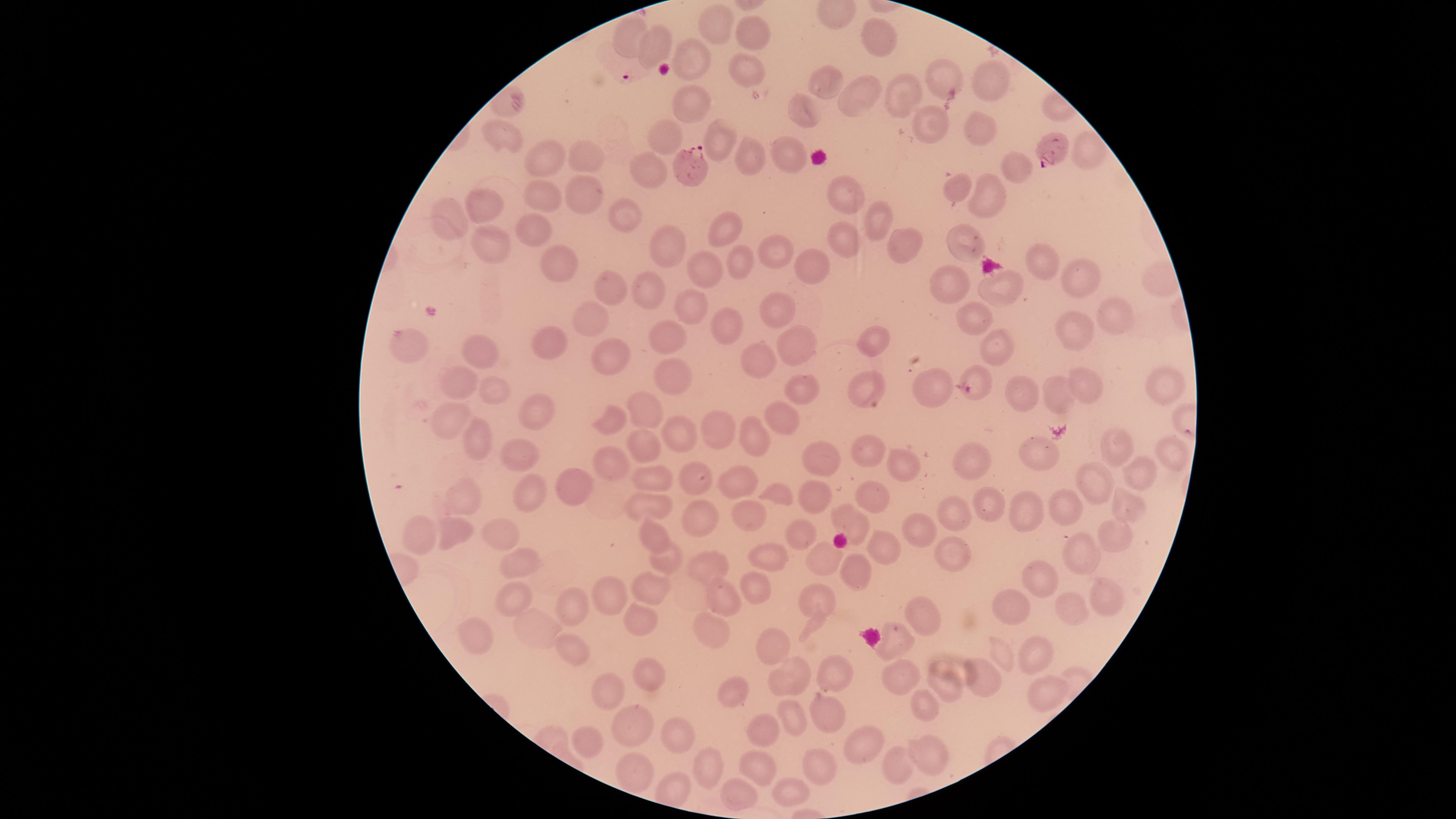
Approximate marker points as {x, y} in pixels. Uninfected RBCs: {716, 24}, {628, 34}, {751, 35}, {882, 37}, {658, 43}, {694, 59}, {746, 70}, {826, 79}, {947, 79}, {991, 81}, {865, 94}, {895, 95}, {691, 106}, {807, 112}, {936, 125}, {981, 126}, {497, 136}, {716, 136}, {662, 137}, {1090, 147}, {790, 151}, {584, 154}, {747, 157}, {546, 161}, {1010, 164}, {653, 172}, {962, 187}, {848, 192}, {580, 193}, {988, 196}, {539, 201}, {486, 205}, {621, 219}, {873, 219}, {453, 222}, {729, 231}, {531, 234}, {847, 236}, {967, 236}, {905, 241}, {494, 242}, {669, 250}, {777, 253}, {1034, 256}, {561, 263}, {738, 263}, {817, 266}, {710, 271}, {1087, 276}, {956, 282}, {1002, 282}, {614, 285}, {657, 286}, {695, 305}, {775, 313}, {975, 315}, {1110, 318}, {589, 324}, {723, 326}, {1075, 330}, {667, 337}, {873, 341}, {792, 343}, {995, 344}, {554, 345}, {410, 348}, {474, 353}, {614, 356}, {762, 359}, {675, 372}, {975, 375}, {1085, 383}, {1156, 383}, {805, 385}, {870, 385}, {461, 386}, {933, 388}, {501, 391}, {1057, 392}, {1023, 393}, {544, 404}, {783, 409}, {649, 410}, {453, 419}, {610, 420}, {714, 437}, {686, 441}, {752, 441}, {477, 443}, {646, 443}, {1115, 448}, {868, 455}, {830, 456}, {1165, 457}, {519, 458}, {616, 462}, {1037, 462}, {982, 466}, {907, 467}, {1135, 474}, {655, 479}, {696, 481}, {738, 482}, {1096, 483}, {574, 488}, {814, 491}, {775, 493}, {870, 493}, {466, 499}, {525, 499}, {650, 504}, {987, 509}, {1024, 509}, {1071, 512}, {752, 513}, {1123, 513}, {851, 514}, {704, 515}, {957, 518}, {426, 528}, {458, 528}, {803, 531}, {503, 532}, {653, 532}, {927, 532}, {1111, 536}, {880, 544}, {771, 550}, {951, 554}, {1079, 554}, {666, 558}, {825, 558}, {517, 563}, {710, 564}, {857, 570}, {1048, 576}, {656, 583}, {757, 583}, {614, 591}, {723, 596}, {510, 597}, {817, 598}, {1073, 602}, {1103, 602}, {1015, 605}, {571, 606}, {640, 621}, {921, 622}, {711, 626}, {537, 628}, {478, 640}, {896, 646}, {573, 648}, {774, 650}, {1035, 651}, {1003, 653}, {831, 676}, {898, 676}, {646, 677}, {983, 679}, {949, 683}, {791, 684}, {729, 689}, {607, 691}, {1045, 691}, {920, 707}, {822, 714}, {794, 717}, {764, 725}, {633, 730}, {589, 737}, {870, 738}, {678, 740}, {929, 750}, {822, 761}, {896, 761}, {761, 763}, {638, 766}, {709, 767}, {793, 783}, {736, 786}. Parasitized RBCs: {1052, 150}, {688, 166}. Image is 1456×819 pixels. Thin smear of blood. Presence: malaria parasites identified. The visible region is circular. Smartphone photograph through the microscope eyepiece. Single field of view. Giemsa stain. Species: Plasmodium falciparum.